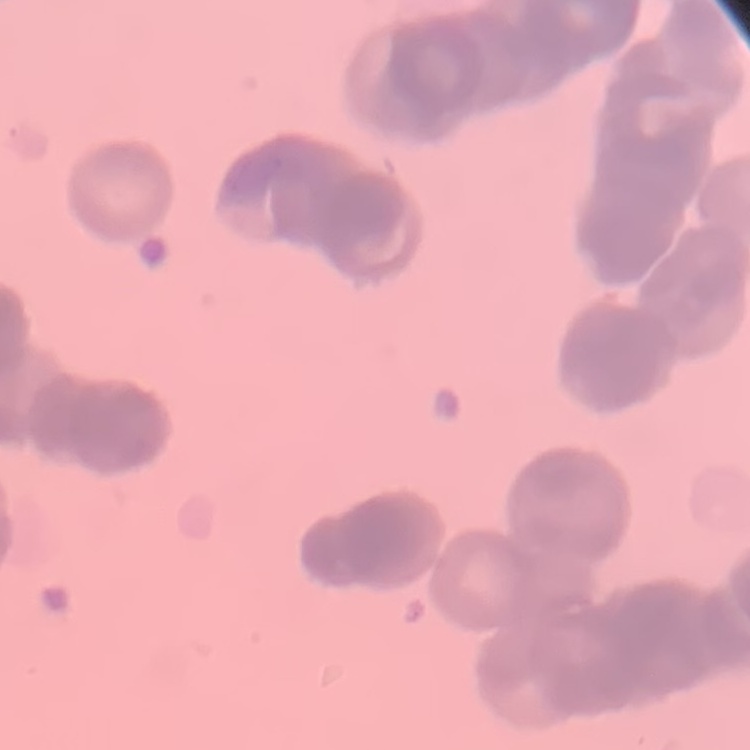
The red blood cells show rouleaux formation. One tile cut from a larger photomicrograph. Thin blood smear. Field's or Giemsa stain.